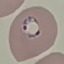

Result: malaria parasites identified. Giemsa-stained preparation. Acquired by smartphone through the microscope eyepiece. Cell patch, automatically extracted from a larger field of view and resized to 64 × 64 pixels. Thin smear of blood.